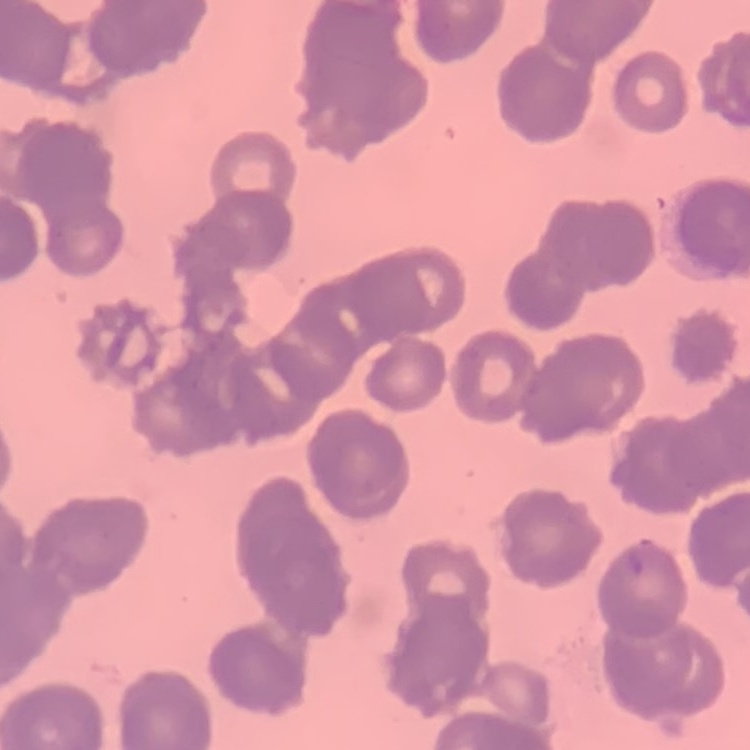

The red blood cells show rouleaux formation. Square crop of a larger photomicrograph. Stained with either Field's or Giemsa. Thin blood film.